State which parasite is depicted.
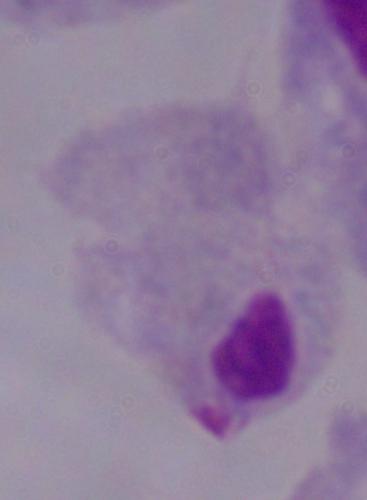
This is a trichomonad.

Photomicrograph. Captured at 1000x magnification.